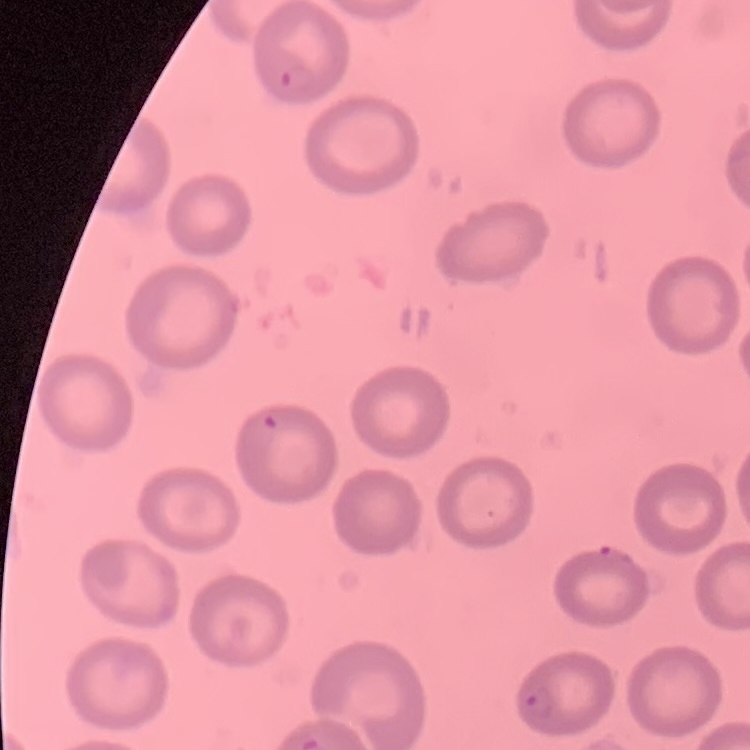
{
  "erythrocyte_morphology": "no rouleaux formation",
  "image_type": "square crop of a larger photomicrograph",
  "stain": "Field's or Giemsa",
  "preparation": "thin blood film"
}